Comment on the morphology of the red blood cells.
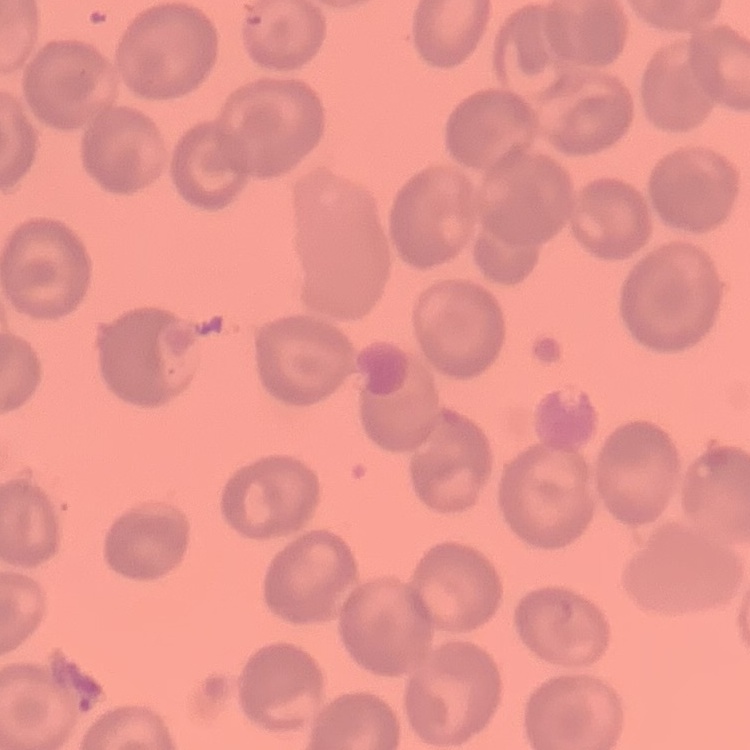

They show no rouleaux formation.

image type = square crop of a larger photomicrograph
preparation = thin peripheral smear
stain = Field's or Giemsa